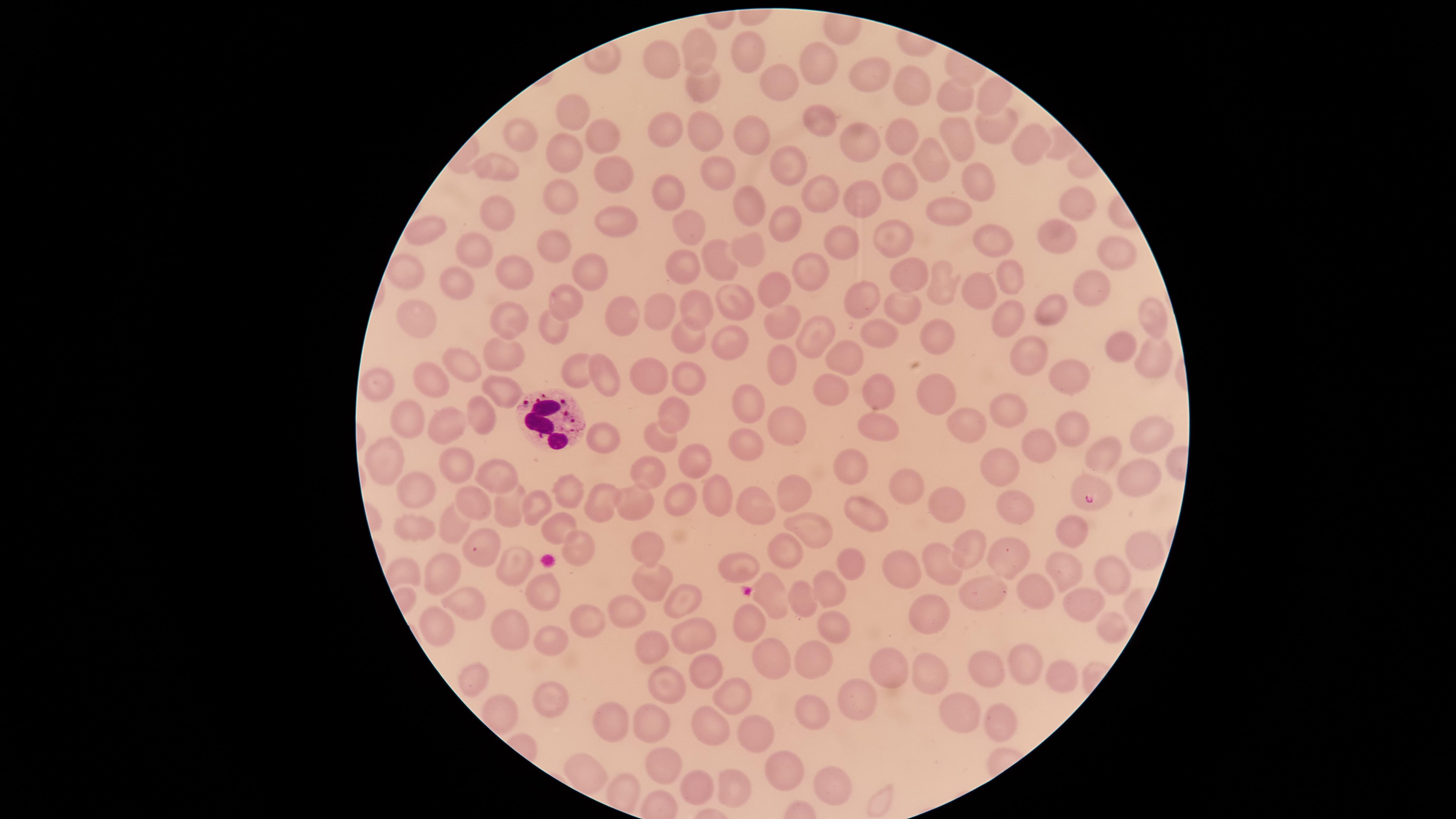

Approximate marker points as (x, y) in pixels. Uninfected RBCs: (742, 50), (702, 53), (818, 57), (660, 59), (868, 74), (780, 82), (698, 83), (916, 90), (957, 97), (991, 99), (571, 101), (818, 119), (998, 126), (517, 129), (902, 130), (707, 132), (749, 132), (667, 133), (959, 134), (600, 135), (860, 139), (1027, 141), (564, 153), (930, 155), (493, 164), (788, 164), (716, 169), (610, 173), (979, 177), (904, 180), (670, 187), (821, 197), (558, 198), (861, 200), (1072, 201), (748, 206), (946, 211), (496, 214), (613, 220), (788, 221), (683, 227), (423, 234), (1049, 235), (893, 237), (993, 240), (842, 242), (465, 245), (754, 247), (1111, 248), (557, 249), (716, 254), (585, 269), (910, 270), (693, 271), (413, 272), (813, 272), (513, 273), (1005, 276), (939, 284), (772, 286), (461, 288), (1090, 288), (975, 290), (865, 297), (741, 299), (691, 303), (568, 305), (902, 305), (1046, 311), (661, 313), (512, 317), (1152, 318), (413, 320), (776, 320), (1010, 320), (621, 324), (816, 325), (551, 329), (691, 331), (935, 332), (882, 336), (729, 339), (1120, 343), (852, 352), (507, 355), (1025, 355), (1159, 357), (460, 359), (783, 368), (573, 369), (431, 378), (610, 378), (694, 378), (1077, 378), (652, 379), (375, 382), (832, 388), (879, 390), (506, 393), (936, 397), (751, 403), (479, 412), (1008, 412), (673, 413), (410, 418), (454, 425), (878, 426), (790, 427), (966, 428), (1150, 428), (1071, 430), (655, 435), (748, 436), (607, 438), (1039, 445), (1104, 454), (704, 461), (458, 462), (386, 463), (851, 463), (996, 466), (647, 470), (1138, 471), (499, 479), (907, 489), (421, 492), (793, 492), (565, 494), (714, 495), (470, 496), (639, 499), (669, 501), (600, 505), (756, 505), (1011, 505), (946, 506), (511, 508), (537, 508), (855, 517), (559, 522), (451, 526), (1066, 528), (418, 529), (808, 531), (646, 544), (580, 546), (966, 547), (483, 551), (1138, 551), (784, 554), (1016, 558), (855, 565), (942, 566), (515, 567), (741, 567), (898, 567), (1066, 569), (1115, 573), (644, 574), (439, 575), (822, 583), (1039, 588), (545, 591), (769, 594), (681, 595), (808, 597), (978, 600), (1079, 600), (467, 607), (925, 609), (629, 613), (589, 617), (834, 618), (747, 622), (1108, 625), (438, 630), (516, 630), (694, 635), (551, 638), (650, 643), (775, 655), (812, 655), (1031, 664), (702, 669), (985, 670), (888, 671), (928, 676), (475, 679), (1063, 679), (666, 687), (733, 691), (552, 697), (852, 699), (809, 706), (958, 714), (657, 720), (712, 723), (996, 723), (757, 737), (659, 758), (786, 775), (693, 784), (833, 785), (733, 788). Parasitized RBCs: (1092, 494). WBCs: (544, 419). Thin blood smear. Species: Plasmodium falciparum. Smartphone photograph through the microscope eyepiece. Presence: malaria parasites detected. Image is 1456×819 pixels. Giemsa-stained preparation. The visible region is circular. One field of view of the specimen.